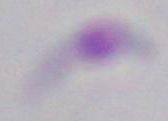

Photomicrograph. Toxoplasma gondii is seen. 1000x magnification.